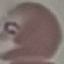

result = malaria parasites identified
preparation = thin blood smear
capture = smartphone camera at the microscope eyepiece
stain = Giemsa
image type = automatically extracted cell patch, resized to 64 × 64 pixels